Report the malaria status of this cell.
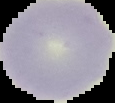

Uninfected.

From a thin blood smear. Image is 115×103 pixels. Segmented cell region on a black background.